Name the blood parasite species.
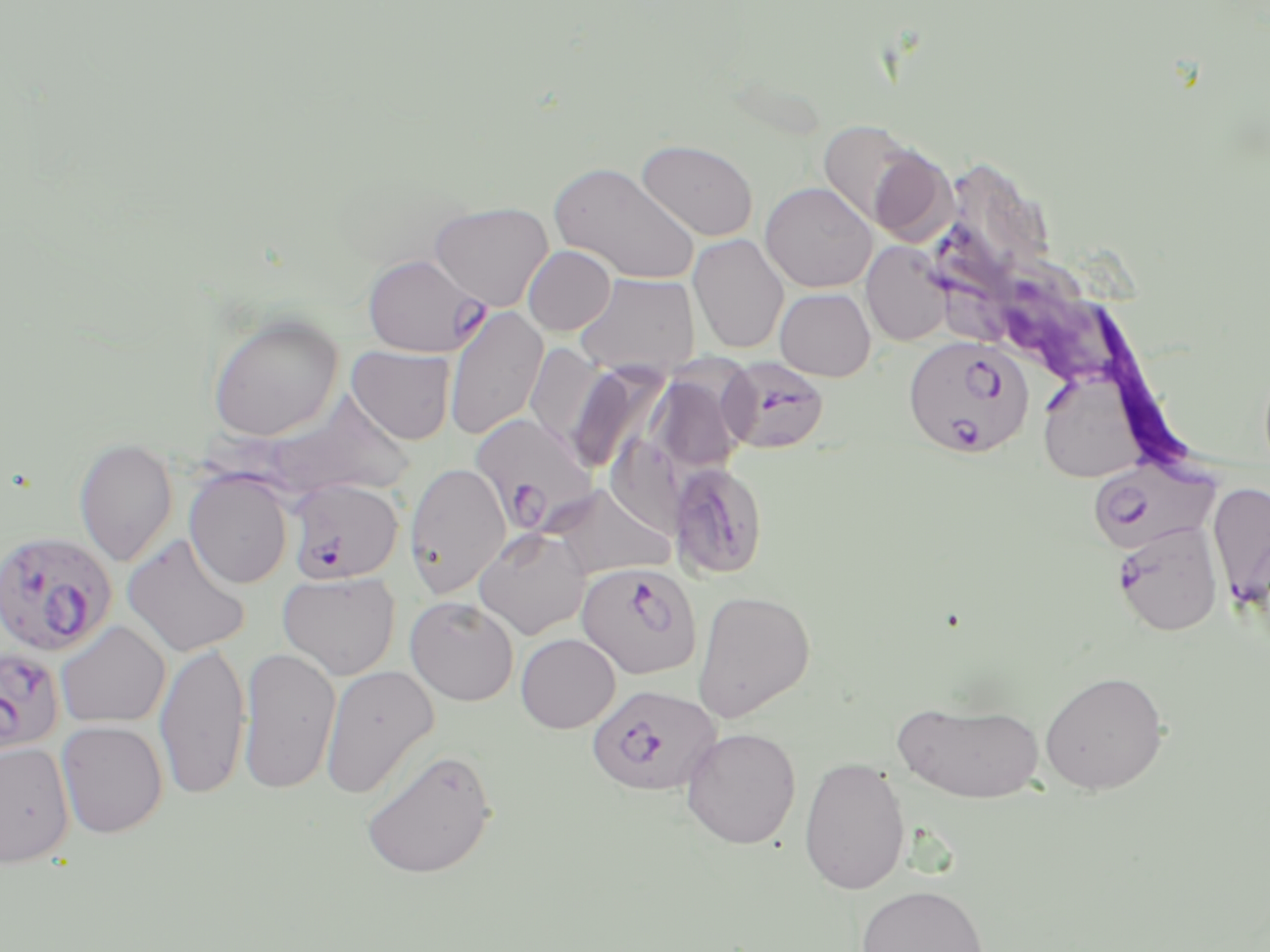

Plasmodium falciparum.

modality: optical microscopy
uninfected_red_blood_cell_locations: 'approximate bounding boxes as named x1/y1/x2/y2 corners in pixels: (x1=814, y1=120, x2=939, y2=234), (x1=636, y1=138, x2=759, y2=242), (x1=550, y1=161, x2=700, y2=285), (x1=760, y1=181, x2=877, y2=293), (x1=430, y1=201, x2=553, y2=310), (x1=688, y1=234, x2=789, y2=354), (x1=861, y1=241, x2=951, y2=346), (x1=523, y1=245, x2=616, y2=335), (x1=573, y1=272, x2=701, y2=377), (x1=774, y1=287, x2=876, y2=382), (x1=444, y1=306, x2=548, y2=441), (x1=208, y1=313, x2=343, y2=441), (x1=525, y1=342, x2=604, y2=450), (x1=346, y1=345, x2=456, y2=444), (x1=565, y1=361, x2=669, y2=475), (x1=648, y1=365, x2=752, y2=474), (x1=1039, y1=380, x2=1143, y2=482), (x1=75, y1=437, x2=178, y2=567), (x1=404, y1=462, x2=511, y2=598), (x1=185, y1=470, x2=293, y2=589), (x1=543, y1=483, x2=676, y2=578), (x1=474, y1=527, x2=591, y2=639), (x1=122, y1=533, x2=251, y2=657), (x1=278, y1=570, x2=401, y2=680), (x1=692, y1=589, x2=816, y2=723), (x1=405, y1=596, x2=519, y2=706), (x1=55, y1=621, x2=171, y2=728), (x1=515, y1=633, x2=620, y2=733), (x1=154, y1=641, x2=250, y2=800), (x1=238, y1=647, x2=341, y2=795), (x1=320, y1=665, x2=439, y2=799), (x1=1039, y1=670, x2=1169, y2=794), (x1=893, y1=698, x2=1046, y2=803), (x1=56, y1=720, x2=168, y2=838), (x1=680, y1=727, x2=801, y2=849), (x1=0, y1=742, x2=74, y2=867), (x1=361, y1=747, x2=497, y2=879), (x1=798, y1=755, x2=910, y2=896), (x1=854, y1=884, x2=989, y2=952)'
stain: May-Grünwald-Giemsa
field_of_view: single
preparation: thin blood film
image_size: 1270×952 pixels
plasmodium_falciparum_infected_red_blood_cell_locations: 'approximate bounding boxes as named x1/y1/x2/y2 corners in pixels: (x1=362, y1=253, x2=489, y2=357), (x1=904, y1=336, x2=1033, y2=459), (x1=720, y1=356, x2=829, y2=454), (x1=471, y1=412, x2=597, y2=533), (x1=1087, y1=457, x2=1219, y2=554), (x1=668, y1=462, x2=768, y2=580), (x1=286, y1=478, x2=403, y2=584), (x1=1207, y1=481, x2=1270, y2=604), (x1=1112, y1=520, x2=1223, y2=637), (x1=0, y1=530, x2=117, y2=656), (x1=577, y1=561, x2=702, y2=680), (x1=0, y1=646, x2=66, y2=757), (x1=586, y1=682, x2=722, y2=797)'
magnification: 1000x